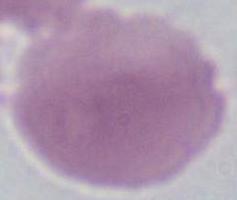 An erythrocyte is seen. 1000x magnification. Photomicrograph.